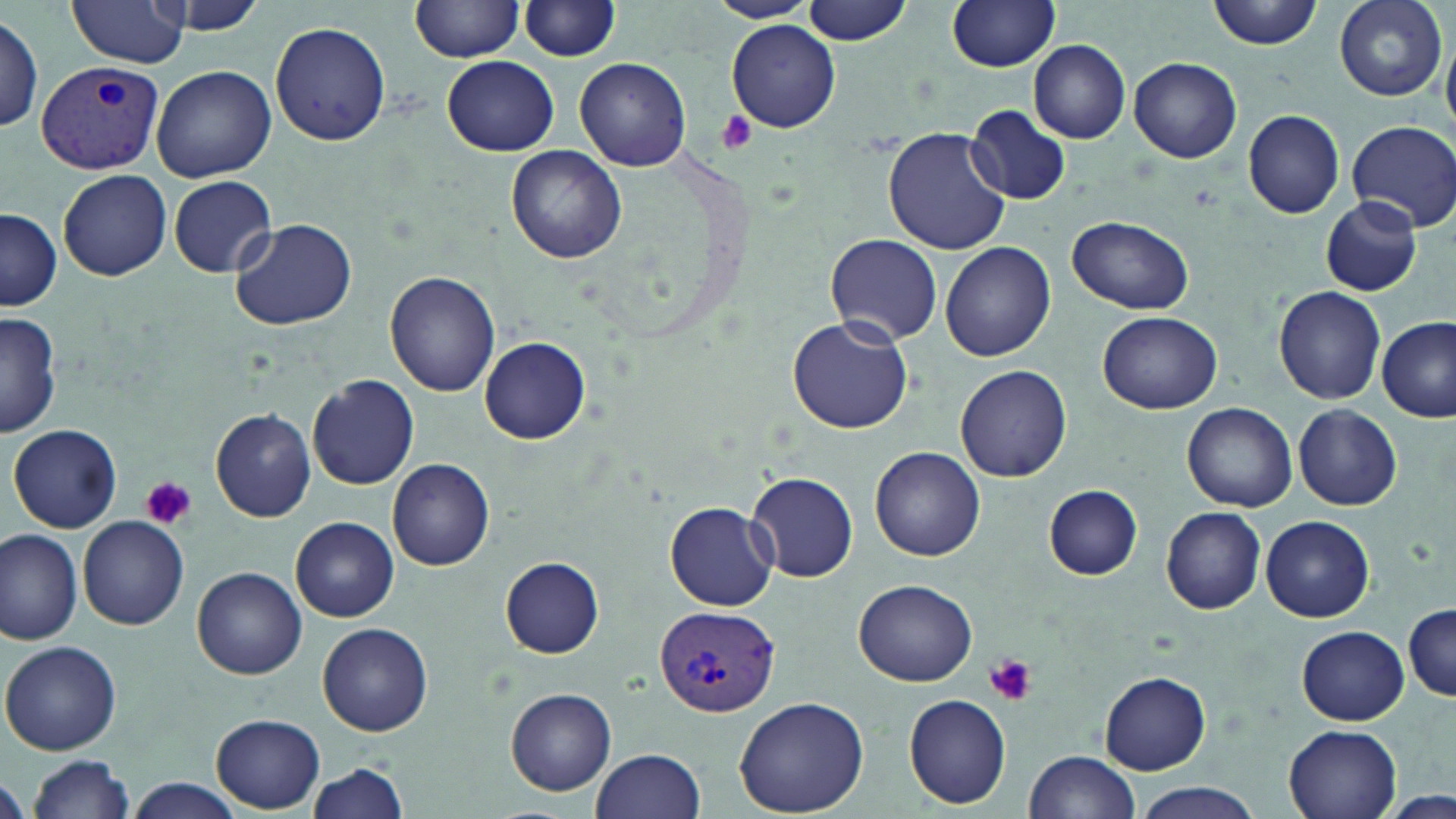

Summary:
  - Coordinate format: approximate bounding boxes as [x1, y1, x2, y2] in pixels
  - Platelet locations: [713, 111, 759, 154], [141, 476, 196, 531], [982, 653, 1039, 707]
  - Uninfected red blood cell locations: [69, 0, 190, 67], [148, 0, 274, 34], [411, 0, 526, 61], [711, 0, 818, 23], [801, 0, 914, 46], [948, 0, 1061, 73], [1210, 0, 1325, 48], [1334, 0, 1446, 100], [520, 1, 622, 62], [1, 12, 44, 134], [727, 20, 841, 133], [271, 22, 392, 145], [1028, 39, 1131, 144], [443, 55, 559, 156], [1129, 57, 1243, 164], [574, 58, 691, 170], [151, 64, 277, 182], [968, 108, 1071, 203], [1243, 109, 1346, 219], [1348, 120, 1456, 232], [884, 129, 1010, 255], [507, 146, 627, 264], [59, 170, 171, 281], [169, 176, 277, 277], [1320, 197, 1421, 295], [0, 207, 61, 310], [228, 216, 358, 330], [1065, 216, 1195, 314], [824, 233, 942, 344], [941, 242, 1056, 362], [384, 271, 501, 396], [1272, 286, 1387, 403], [0, 310, 62, 439], [1098, 311, 1222, 414], [786, 317, 913, 433], [1377, 317, 1454, 422], [480, 336, 589, 444], [955, 363, 1072, 482], [308, 374, 419, 489], [1182, 402, 1298, 513], [1293, 403, 1402, 511], [210, 408, 315, 521], [9, 424, 122, 533], [871, 446, 985, 561], [387, 459, 495, 570], [744, 471, 859, 583], [1044, 485, 1143, 579], [666, 503, 777, 610], [1160, 506, 1267, 615], [79, 515, 188, 631], [1260, 515, 1374, 622], [291, 516, 398, 621], [0, 527, 83, 643], [500, 556, 606, 658], [193, 567, 306, 679], [853, 579, 978, 687], [1403, 605, 1456, 702], [318, 621, 432, 736], [1297, 625, 1408, 724], [0, 640, 122, 754], [1100, 671, 1211, 775], [505, 688, 617, 796], [903, 692, 1012, 809], [733, 695, 870, 817], [211, 714, 325, 811], [1284, 724, 1403, 819], [591, 747, 706, 819], [1024, 750, 1139, 819], [27, 756, 134, 819], [305, 761, 410, 819], [1, 775, 29, 819], [129, 778, 245, 818], [1130, 785, 1264, 819]
  - Plasmodium vivax-infected red blood cell locations: [34, 58, 164, 174], [654, 603, 780, 716]
  - Slide-level diagnosis: Plasmodium vivax
  - Image size: 1456×819 pixels
  - Field of view: one of a larger specimen
  - Preparation: thin blood smear
  - Modality: optical microscopy
  - Stain: May-Grünwald-Giemsa
  - Magnification: 1000x